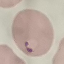

result = malaria parasites identified
image type = cell patch, automatically extracted from a larger field of view and resized to 64 × 64 pixels
capture = smartphone camera at the microscope eyepiece
preparation = thin blood smear
stain = Giemsa